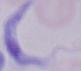

Summary:
  - Modality: photomicrograph
  - Magnification: 1000x
  - Identification: trypanosome